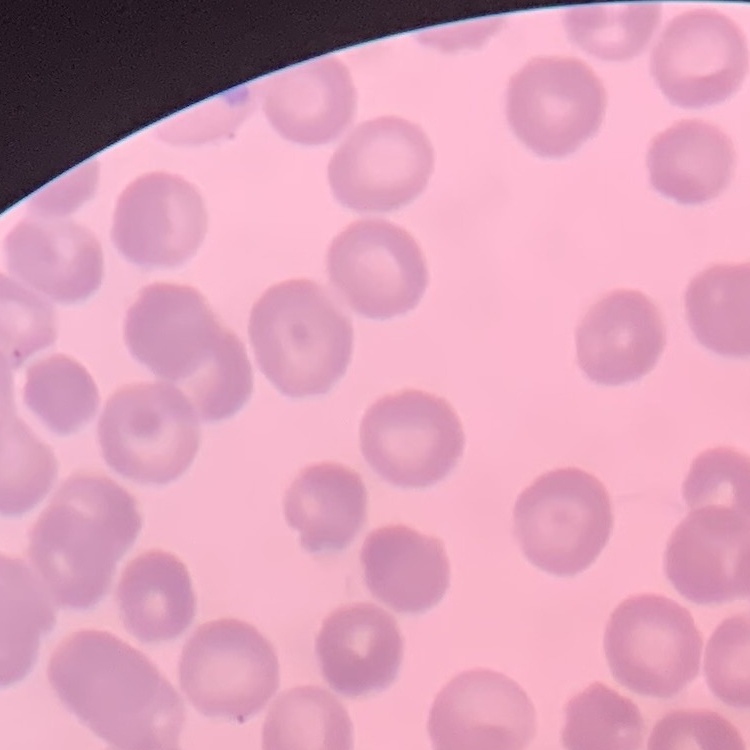
erythrocyte morphology = no rouleaux formation
image type = square crop of a larger photomicrograph
preparation = thin peripheral smear
stain = Field's or Giemsa